Identify the preparation type.
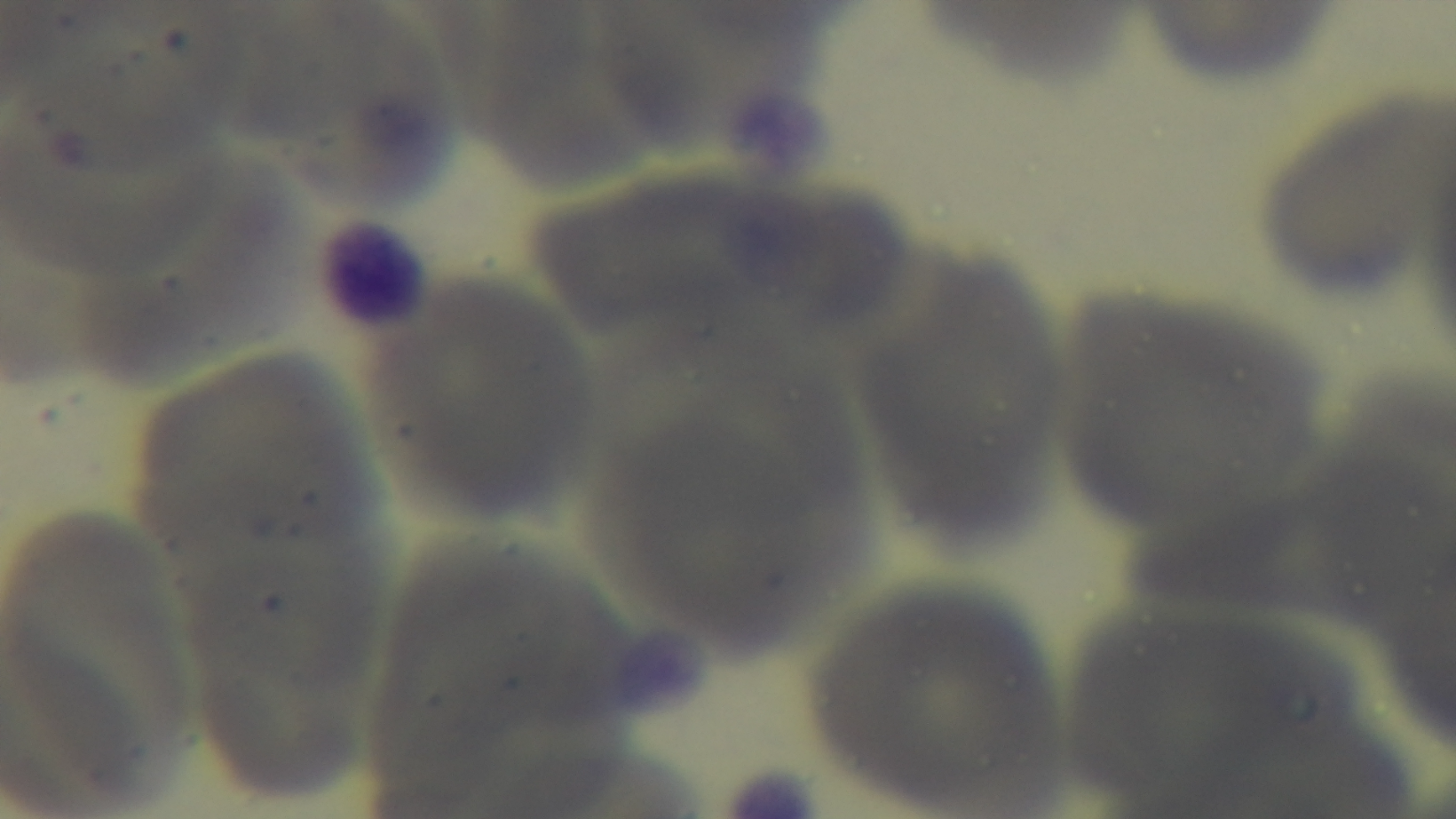
A thin smear.

Mounted 4K digital camera. Oil-immersion objective, 100x. Malaria status: uninfected. Single field of view. Light microscopy. Giemsa stain.